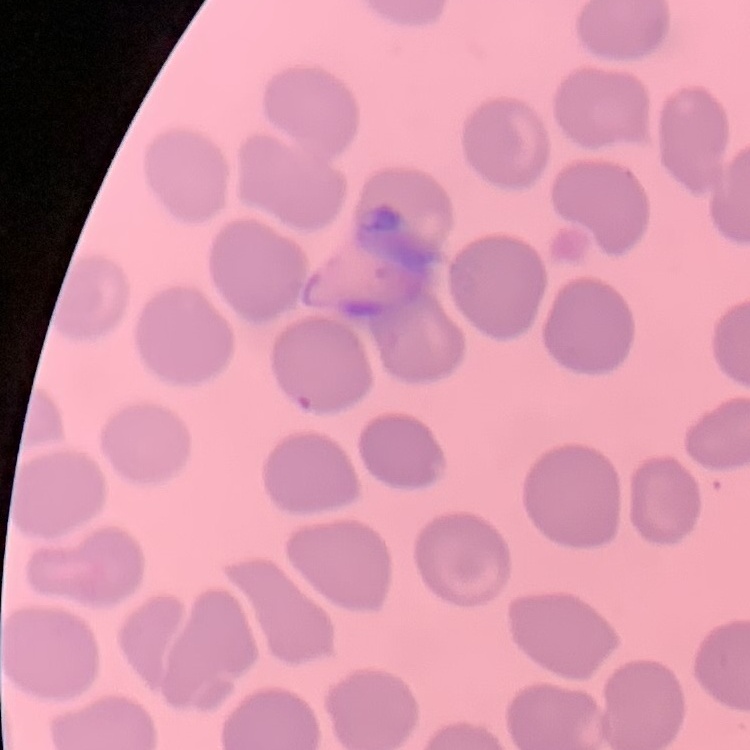 The erythrocytes exhibit no rouleaux formation. Field's or Giemsa stain. One tile cut from a larger photomicrograph. Thin blood smear.